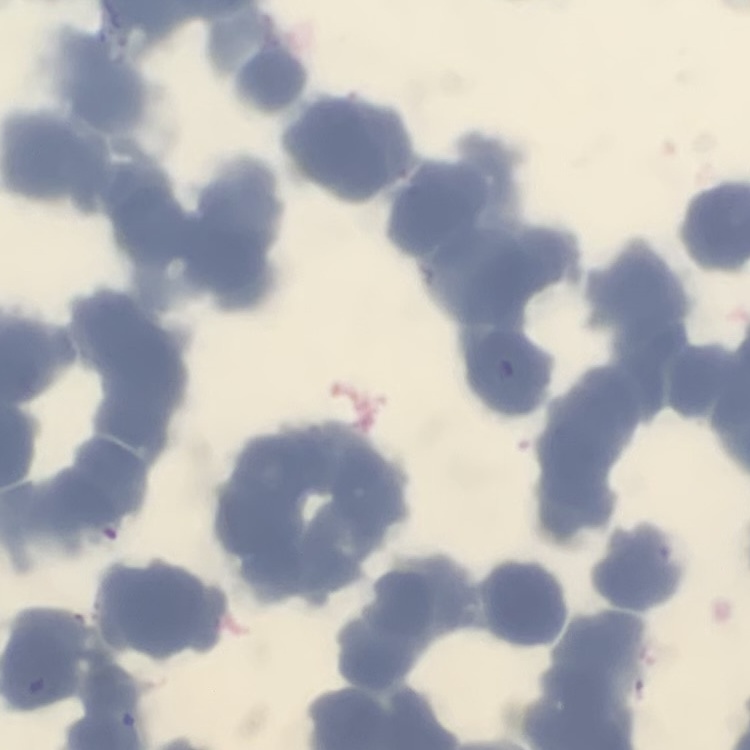

Summary:
  - Erythrocyte morphology: rouleaux formation
  - Stain: Field's or Giemsa
  - Preparation: thin peripheral smear
  - Image type: one tile cut from a larger photomicrograph